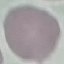

Malaria status: uninfected. Photographed with a smartphone camera at the microscope eyepiece. Thin blood film. Cell patch, automatically extracted from a larger field of view and resized to 64 × 64 pixels. Giemsa-stained preparation.